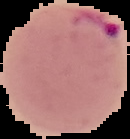
Result: Plasmodium parasites detected. Image is 130×139 pixels. From a thin blood smear. Segmented cell region on a black background.